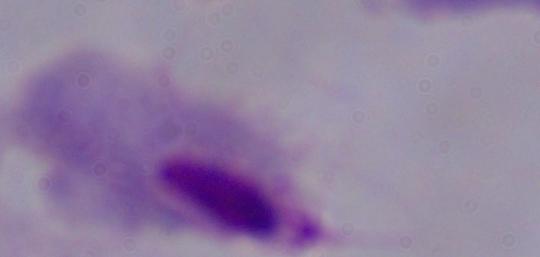

Summary:
  - Identification: trichomonad
  - Modality: micrograph
  - Magnification: 1000x